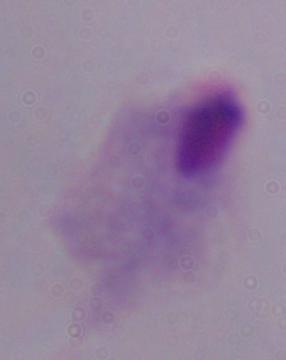

magnification = 1000x
modality = photomicrograph
identification = trichomonad